Report the malaria status of this cell.
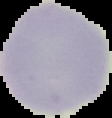

Uninfected.

Image is 112×118 pixels. From a thin blood film. Segmented cell region on a black background.